Report the malaria status of this cell.
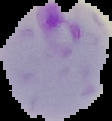
It is parasitized.

Summary:
  - Image type: cell region segmented out of the field of view; surrounding area masked to black
  - Preparation: thin blood smear
  - Image size: 112×121 pixels